Evaluate for malaria.
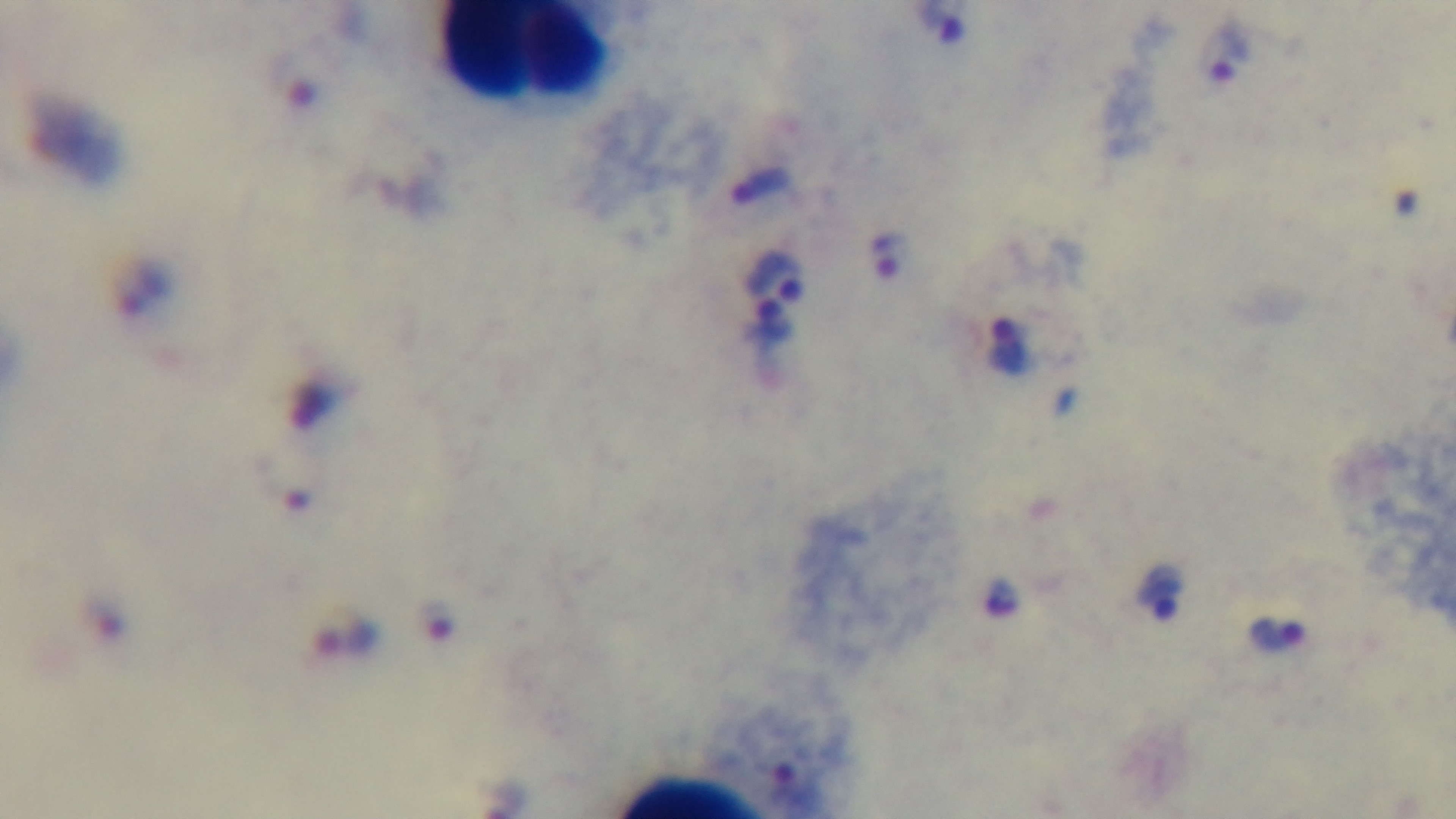
Positive.

Summary:
  - Preparation: thick smear
  - Stain: Giemsa
  - Field of view: one from the slide
  - Capture: mounted 4K digital camera
  - Objective: 100x oil immersion
  - Modality: light microscopy